Outline each blood parasite and name the species.
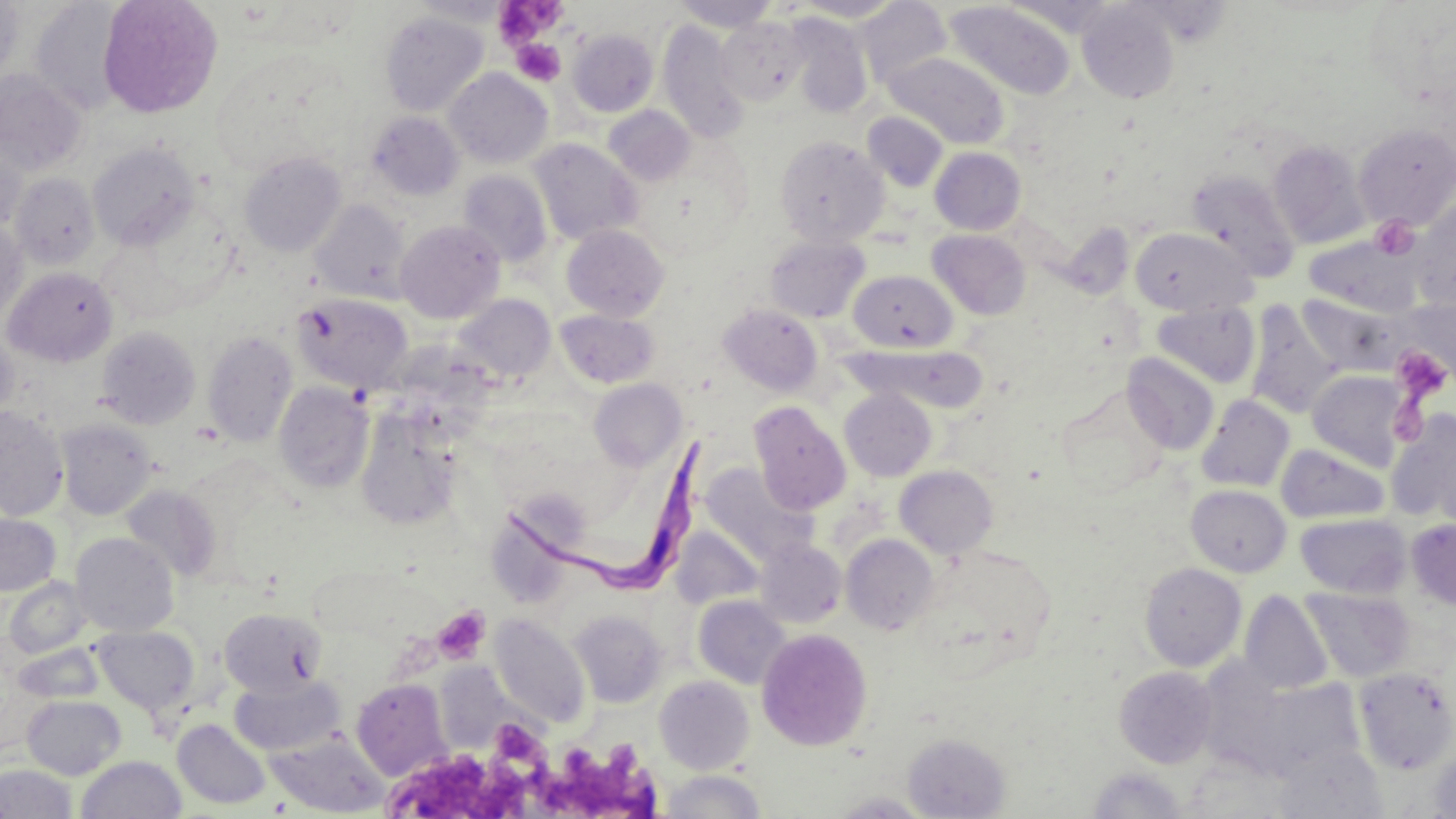

Approximate bounding boxes as named x1/y1/x2/y2 corners in pixels.
Trypanosoma brucei: (x1=501, y1=435, x2=709, y2=608).
No Plasmodium falciparum, Plasmodium ovale, Plasmodium malariae, Plasmodium vivax, or Babesia divergens observed.

Platelet locations: (x1=492, y1=2, x2=567, y2=46), (x1=511, y1=39, x2=565, y2=86), (x1=1370, y1=215, x2=1419, y2=259), (x1=1391, y1=346, x2=1452, y2=402), (x1=432, y1=609, x2=489, y2=664), (x1=493, y1=720, x2=539, y2=761), (x1=528, y1=743, x2=660, y2=819), (x1=391, y1=749, x2=532, y2=819). Uninfected red blood cell locations: (x1=0, y1=0, x2=22, y2=89), (x1=410, y1=0, x2=512, y2=24), (x1=792, y1=0, x2=905, y2=22), (x1=30, y1=1, x2=129, y2=116), (x1=98, y1=1, x2=222, y2=117), (x1=670, y1=1, x2=779, y2=31), (x1=855, y1=2, x2=951, y2=89), (x1=945, y1=2, x2=1076, y2=100), (x1=1077, y1=2, x2=1180, y2=104), (x1=1366, y1=4, x2=1456, y2=103), (x1=380, y1=11, x2=489, y2=117), (x1=787, y1=13, x2=872, y2=117), (x1=716, y1=17, x2=808, y2=105), (x1=657, y1=20, x2=750, y2=144), (x1=568, y1=28, x2=658, y2=116), (x1=885, y1=52, x2=1009, y2=150), (x1=445, y1=69, x2=553, y2=169), (x1=0, y1=70, x2=86, y2=175), (x1=603, y1=105, x2=695, y2=185), (x1=366, y1=111, x2=464, y2=200), (x1=862, y1=111, x2=948, y2=192), (x1=1354, y1=123, x2=1456, y2=228), (x1=774, y1=136, x2=888, y2=247), (x1=0, y1=137, x2=29, y2=233), (x1=529, y1=138, x2=641, y2=244), (x1=1267, y1=140, x2=1369, y2=249), (x1=88, y1=143, x2=200, y2=250), (x1=930, y1=147, x2=1026, y2=235), (x1=239, y1=152, x2=346, y2=256), (x1=1186, y1=169, x2=1300, y2=281), (x1=456, y1=170, x2=552, y2=267), (x1=9, y1=173, x2=100, y2=269), (x1=311, y1=199, x2=411, y2=302), (x1=1411, y1=202, x2=1456, y2=313), (x1=0, y1=219, x2=28, y2=325), (x1=395, y1=220, x2=505, y2=324), (x1=1060, y1=222, x2=1135, y2=298), (x1=562, y1=225, x2=669, y2=321), (x1=1129, y1=227, x2=1256, y2=316), (x1=928, y1=229, x2=1031, y2=320), (x1=765, y1=235, x2=869, y2=323), (x1=1304, y1=235, x2=1419, y2=315), (x1=3, y1=267, x2=118, y2=366), (x1=848, y1=270, x2=957, y2=352), (x1=293, y1=293, x2=413, y2=393), (x1=1298, y1=293, x2=1401, y2=376), (x1=452, y1=294, x2=557, y2=385), (x1=1152, y1=302, x2=1260, y2=388), (x1=718, y1=303, x2=824, y2=396), (x1=1245, y1=303, x2=1342, y2=418), (x1=555, y1=309, x2=659, y2=388), (x1=96, y1=326, x2=201, y2=429), (x1=0, y1=330, x2=19, y2=428), (x1=203, y1=330, x2=298, y2=446), (x1=858, y1=345, x2=990, y2=413), (x1=1123, y1=353, x2=1220, y2=454), (x1=1307, y1=370, x2=1411, y2=471), (x1=588, y1=378, x2=686, y2=469), (x1=274, y1=381, x2=374, y2=493), (x1=840, y1=388, x2=936, y2=481), (x1=1056, y1=391, x2=1167, y2=497), (x1=1196, y1=394, x2=1295, y2=493), (x1=749, y1=401, x2=851, y2=515), (x1=0, y1=407, x2=69, y2=521), (x1=356, y1=410, x2=462, y2=531), (x1=1387, y1=410, x2=1456, y2=526), (x1=56, y1=419, x2=158, y2=520), (x1=1276, y1=444, x2=1389, y2=524), (x1=699, y1=462, x2=817, y2=566), (x1=895, y1=465, x2=999, y2=558), (x1=122, y1=484, x2=223, y2=581), (x1=1186, y1=484, x2=1291, y2=577), (x1=489, y1=490, x2=589, y2=605), (x1=0, y1=513, x2=61, y2=596), (x1=1296, y1=513, x2=1410, y2=598), (x1=1406, y1=519, x2=1456, y2=610), (x1=671, y1=526, x2=764, y2=610), (x1=70, y1=533, x2=179, y2=637), (x1=841, y1=533, x2=939, y2=635), (x1=754, y1=539, x2=847, y2=628), (x1=916, y1=546, x2=1057, y2=674), (x1=1138, y1=562, x2=1246, y2=672), (x1=3, y1=576, x2=92, y2=659), (x1=1302, y1=588, x2=1415, y2=682), (x1=1238, y1=590, x2=1334, y2=695), (x1=693, y1=595, x2=791, y2=688), (x1=219, y1=608, x2=327, y2=697), (x1=569, y1=610, x2=666, y2=707), (x1=489, y1=613, x2=590, y2=727), (x1=93, y1=625, x2=199, y2=715), (x1=756, y1=627, x2=873, y2=751), (x1=13, y1=641, x2=104, y2=703), (x1=1113, y1=666, x2=1218, y2=768), (x1=1354, y1=667, x2=1456, y2=774), (x1=229, y1=674, x2=346, y2=756), (x1=654, y1=676, x2=754, y2=774), (x1=1234, y1=677, x2=1369, y2=780), (x1=351, y1=678, x2=452, y2=780), (x1=22, y1=695, x2=126, y2=780), (x1=173, y1=719, x2=271, y2=809), (x1=902, y1=732, x2=1010, y2=818), (x1=266, y1=733, x2=388, y2=816), (x1=1272, y1=742, x2=1388, y2=818), (x1=1428, y1=748, x2=1455, y2=818), (x1=76, y1=755, x2=186, y2=819), (x1=0, y1=763, x2=77, y2=819), (x1=1086, y1=767, x2=1192, y2=817), (x1=657, y1=770, x2=767, y2=818). Slide-level diagnosis: Trypanosoma brucei. 1000x magnification. Optical microscopy. Image is 1456×819 pixels. May-Grünwald-Giemsa stain. Thin blood film. One field of a larger specimen.